Give the extent of all Plasmodium falciparum-infected red blood cells.
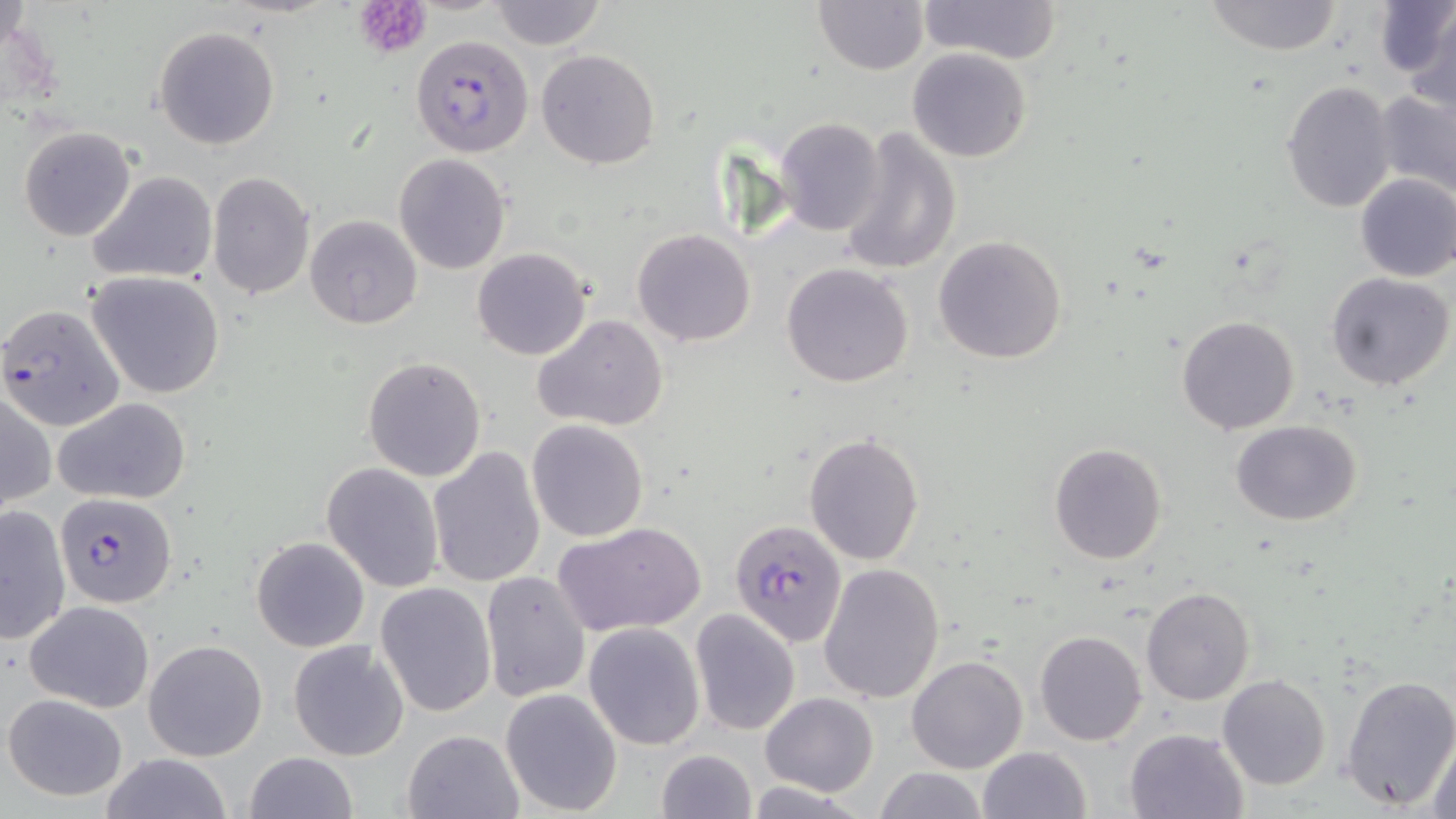
Approximate bounding boxes as [x1, y1, x2, y2] in pixels.
Plasmodium falciparum-infected red blood cells: [411, 34, 535, 156], [0, 304, 124, 431], [55, 491, 177, 608], [729, 519, 847, 648].

slide-level diagnosis = Plasmodium falciparum
uninfected red blood cell locations = approximate bounding boxes as [x1, y1, x2, y2] in pixels: [488, 0, 605, 48], [811, 0, 929, 74], [922, 0, 1062, 64], [1374, 0, 1452, 84], [1202, 1, 1345, 56], [1402, 6, 1456, 117], [154, 25, 280, 150], [905, 47, 1033, 163], [537, 50, 659, 169], [1280, 80, 1397, 212], [1373, 87, 1456, 199], [776, 118, 885, 236], [20, 126, 135, 242], [839, 128, 962, 276], [393, 154, 510, 274], [87, 170, 219, 285], [208, 172, 314, 299], [1353, 172, 1456, 281], [304, 215, 422, 330], [632, 228, 757, 347], [932, 236, 1066, 363], [472, 247, 592, 360], [780, 263, 914, 387], [87, 270, 226, 398], [1327, 272, 1453, 390], [532, 313, 669, 432], [1176, 314, 1302, 434], [362, 357, 487, 482], [1, 390, 54, 513], [53, 397, 191, 505], [1231, 419, 1362, 526], [526, 420, 649, 541], [804, 432, 926, 565], [1047, 443, 1167, 566], [427, 446, 544, 588], [321, 462, 445, 592], [1, 504, 71, 644], [555, 522, 704, 639], [251, 536, 370, 651], [818, 563, 945, 703], [481, 571, 591, 703], [375, 581, 497, 717], [1140, 586, 1254, 706], [24, 601, 154, 712], [689, 608, 801, 736], [583, 623, 705, 749], [1035, 629, 1147, 746], [143, 638, 269, 761], [287, 639, 409, 761], [906, 655, 1028, 774], [1341, 673, 1456, 810], [1217, 675, 1331, 791], [500, 688, 623, 816], [759, 691, 877, 796], [3, 693, 128, 801], [1124, 727, 1248, 818], [402, 729, 523, 818], [1428, 732, 1456, 819], [977, 746, 1091, 819], [654, 748, 758, 819], [243, 752, 359, 819], [99, 753, 233, 819], [872, 766, 988, 819]
magnification = 1000x
image size = 1456×819 pixels
modality = light microscopy
field of view = one of a larger specimen
preparation = thin blood smear
platelet locations = approximate bounding boxes as [x1, y1, x2, y2] in pixels: [354, 0, 434, 58]
stain = May-Grünwald-Giemsa